Report the malaria status of this cell.
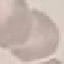

Uninfected.

Summary:
  - Stain: Giemsa
  - Preparation: thin smear
  - Capture: smartphone camera at the microscope eyepiece
  - Image type: cell patch, automatically extracted from a larger field of view and resized to 64 × 64 pixels